Report the malaria status of this cell.
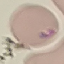
Parasitized.

preparation = thin smear
capture = smartphone through the microscope eyepiece
image type = automatically extracted cell patch, resized to 64 × 64 pixels
stain = Giemsa